Classify this cell by malaria status.
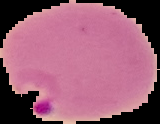
Parasitized.

image type = segmented cell region on a black background
image size = 160×124 pixels
preparation = thin blood film